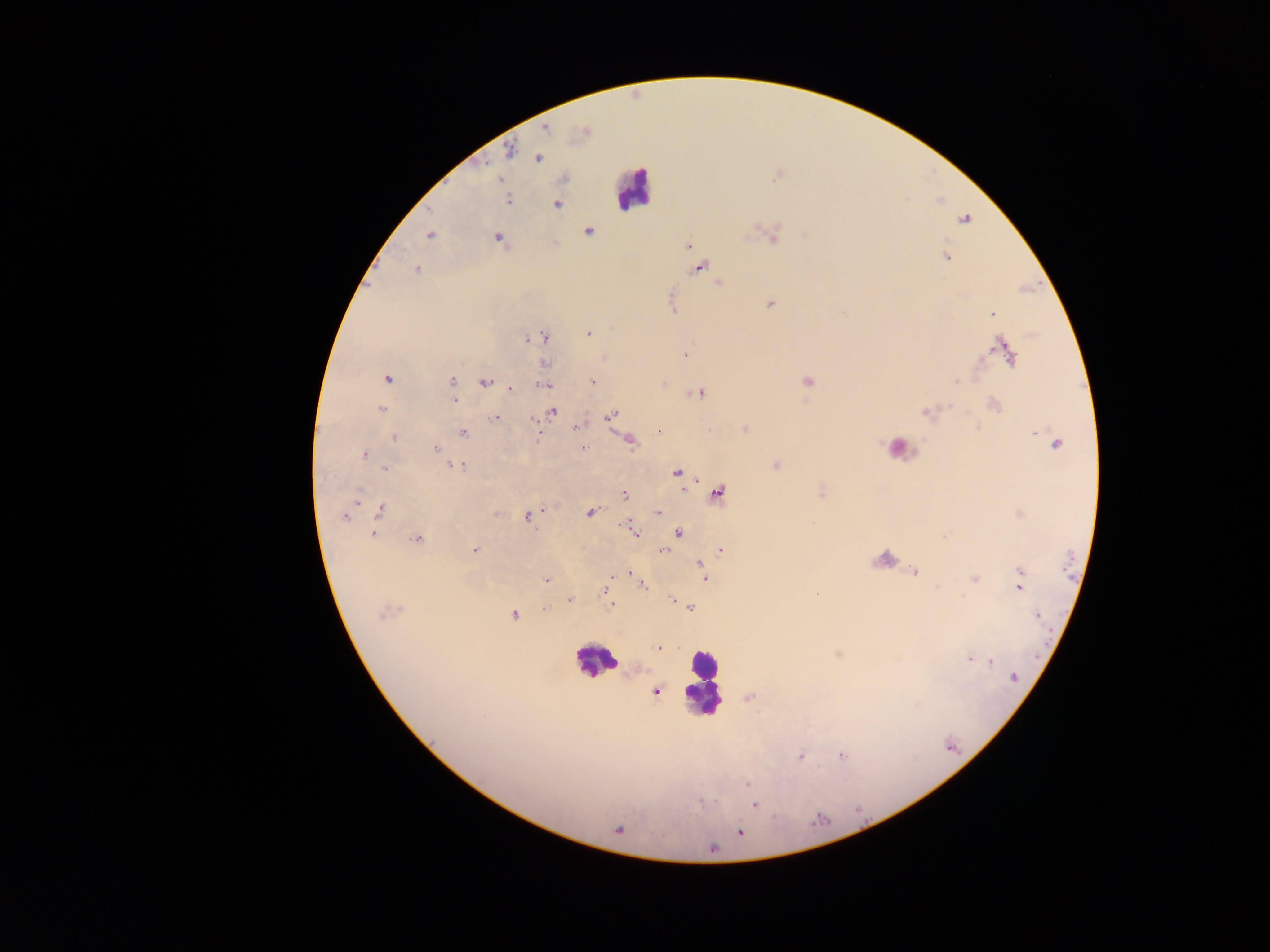 Approximate centers as {x, y} in pixels. Malaria parasite locations: {546, 128}, {582, 131}, {509, 151}, {537, 158}, {500, 179}, {508, 200}, {557, 203}, {963, 219}, {588, 231}, {430, 235}, {771, 236}, {498, 238}, {687, 246}, {946, 257}, {698, 267}, {415, 269}, {718, 283}, {770, 304}, {991, 313}, {588, 333}, {542, 336}, {529, 338}, {1000, 345}, {1006, 351}, {685, 354}, {604, 358}, {545, 363}, {386, 379}, {452, 381}, {806, 381}, {485, 382}, {592, 382}, {662, 383}, {543, 384}, {453, 387}, {510, 389}, {698, 392}, {454, 400}, {993, 404}, {381, 409}, {551, 411}, {927, 411}, {610, 414}, {495, 417}, {534, 423}, {577, 427}, {743, 429}, {659, 431}, {462, 432}, {538, 432}, {1037, 432}, {395, 437}, {628, 440}, {1057, 444}, {582, 448}, {435, 449}, {364, 454}, {775, 464}, {458, 465}, {384, 468}, {677, 473}, {820, 492}, {716, 493}, {624, 494}, {379, 509}, {590, 511}, {496, 513}, {657, 513}, {1020, 514}, {345, 515}, {528, 516}, {630, 526}, {634, 531}, {678, 532}, {373, 534}, {417, 539}, {720, 549}, {474, 550}, {663, 550}, {700, 563}, {914, 572}, {629, 573}, {1020, 573}, {611, 575}, {704, 575}, {973, 578}, {546, 579}, {640, 583}, {1019, 586}, {606, 590}, {570, 599}, {672, 600}, {612, 605}, {543, 608}, {690, 608}, {388, 610}, {513, 614}, {1037, 615}, {658, 648}, {969, 660}, {988, 660}, {1012, 676}, {655, 691}, {748, 697}, {841, 755}, {799, 756}, {747, 783}, {754, 804}, {617, 829}, {739, 831}. Leukocyte locations: {633, 189}, {898, 448}, {883, 558}, {595, 660}, {703, 682}. Single field of view. Thick blood smear. Photographed through a microscope with a mobile-phone camera. Image is 1270×952 pixels. Sample from Ghana.